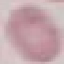

Summary:
  - Result: negative for malaria parasites
  - Image type: cell patch, automatically extracted from a larger field of view and resized to 64 × 64 pixels
  - Stain: Giemsa
  - Capture: smartphone camera at the microscope eyepiece
  - Preparation: thin smear